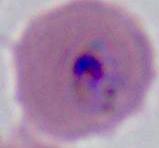

Summary:
  - Magnification: 400x or 1000x
  - Modality: micrograph
  - Identification: Plasmodium